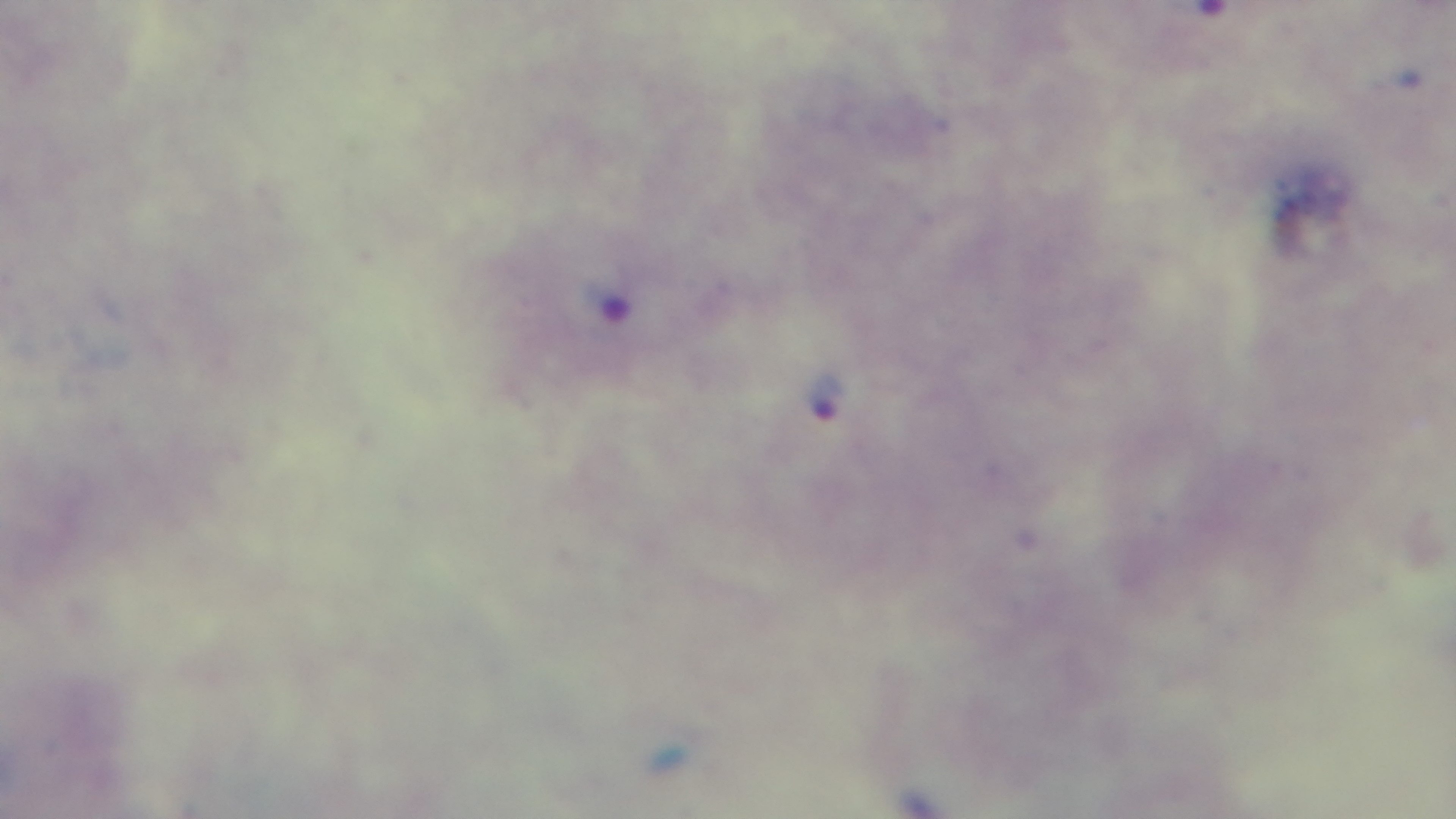

Malaria status: positive. Preparation: thick smear. Giemsa-stained. Light microscopy. 100x oil-immersion objective. Single field of view. Mounted 4K digital camera.